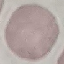
result = negative for malaria parasites
capture = smartphone camera at the microscope eyepiece
image type = cell patch, automatically extracted from a larger field of view and resized to 64 × 64 pixels
stain = Giemsa
preparation = thin smear